State the preparation type.
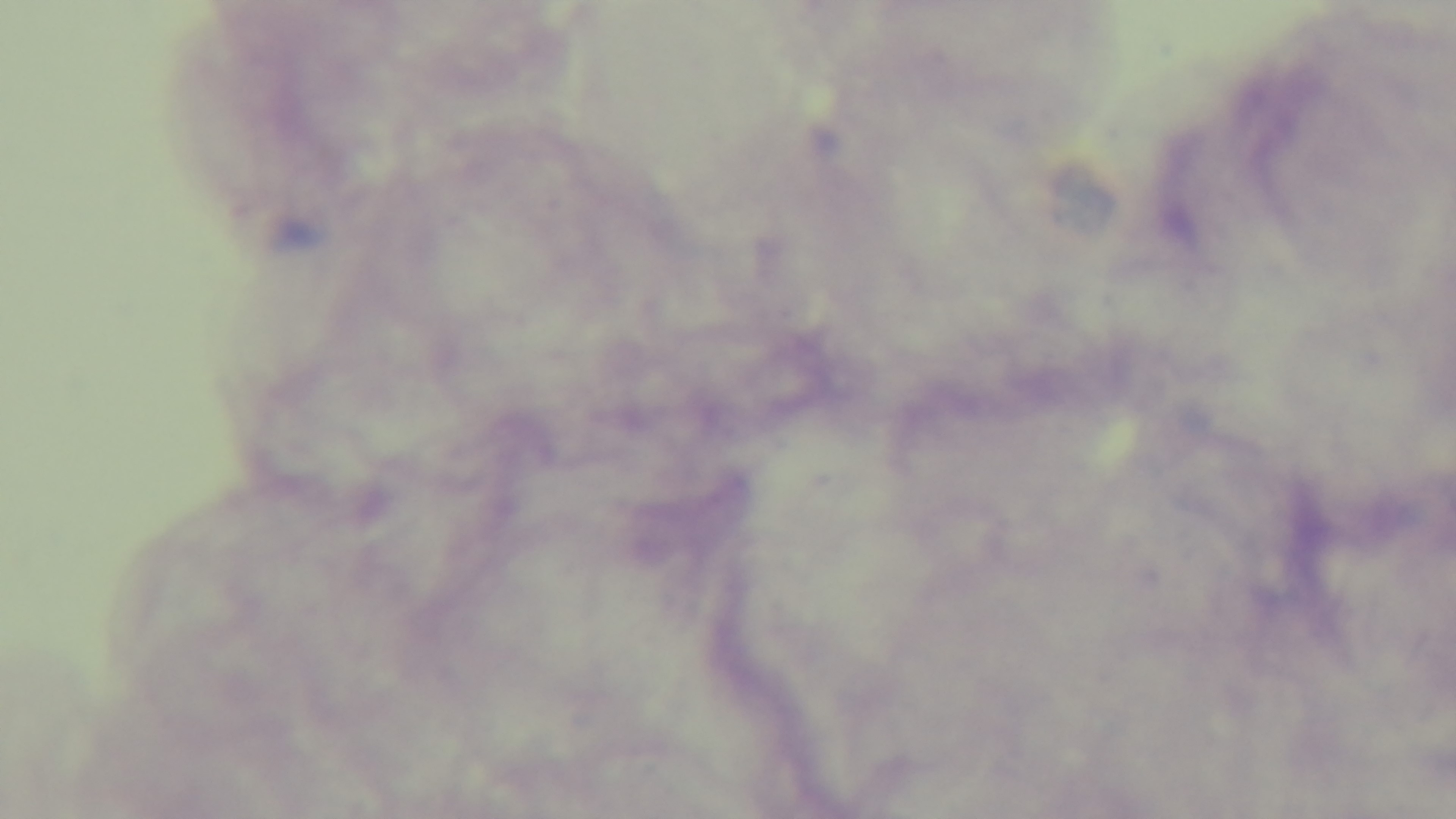

A thick smear.

{
  "capture": "mounted 4K digital camera",
  "field_of_view": "one from the slide",
  "objective": "100x oil immersion",
  "modality": "light microscopy",
  "malaria_status": "negative",
  "stain": "Giemsa"
}